Classify this cell by malaria status.
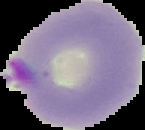
It is parasitized.

From a thin blood smear. Image is 145×130 pixels. Cell region segmented out of the field of view; the surrounding area is masked to black.